Point out each leukocyte.
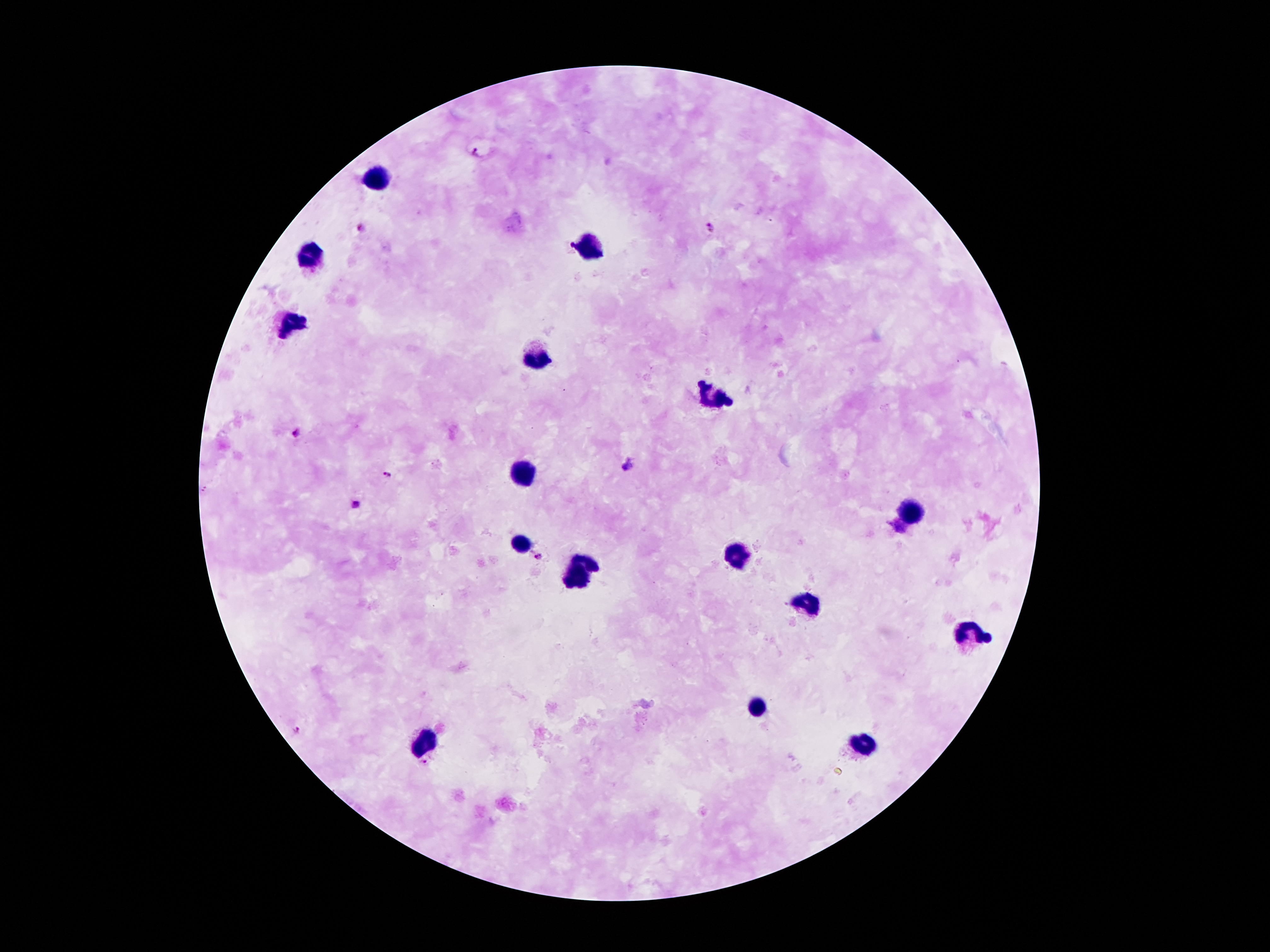
Approximate centers as {x, y} in pixels.
Leukocytes: {376, 178}, {588, 246}, {311, 252}, {294, 322}, {534, 356}, {711, 396}, {524, 473}, {912, 512}, {522, 544}, {737, 554}, {589, 560}, {578, 578}, {808, 604}, {969, 635}, {756, 709}, {422, 741}, {865, 743}.

preparation: thick blood smear
patient_malaria_status: infected with Plasmodium falciparum
image_size: 1270×952 pixels
stain: Giemsa
field_of_view: single
capture: smartphone camera through the microscope eyepiece
magnification: 100x
malaria_parasite_locations: 'approximate centers as {x, y} in pixels: {477, 152}, {360, 228}, {711, 228}, {296, 432}, {627, 462}, {388, 473}, {355, 502}, {538, 555}, {295, 729}, {425, 760}'